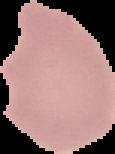

image_size: 115×154 pixels
result: negative for malaria parasites
image_type: segmented cell region with the area outside set to black
preparation: thin blood smear